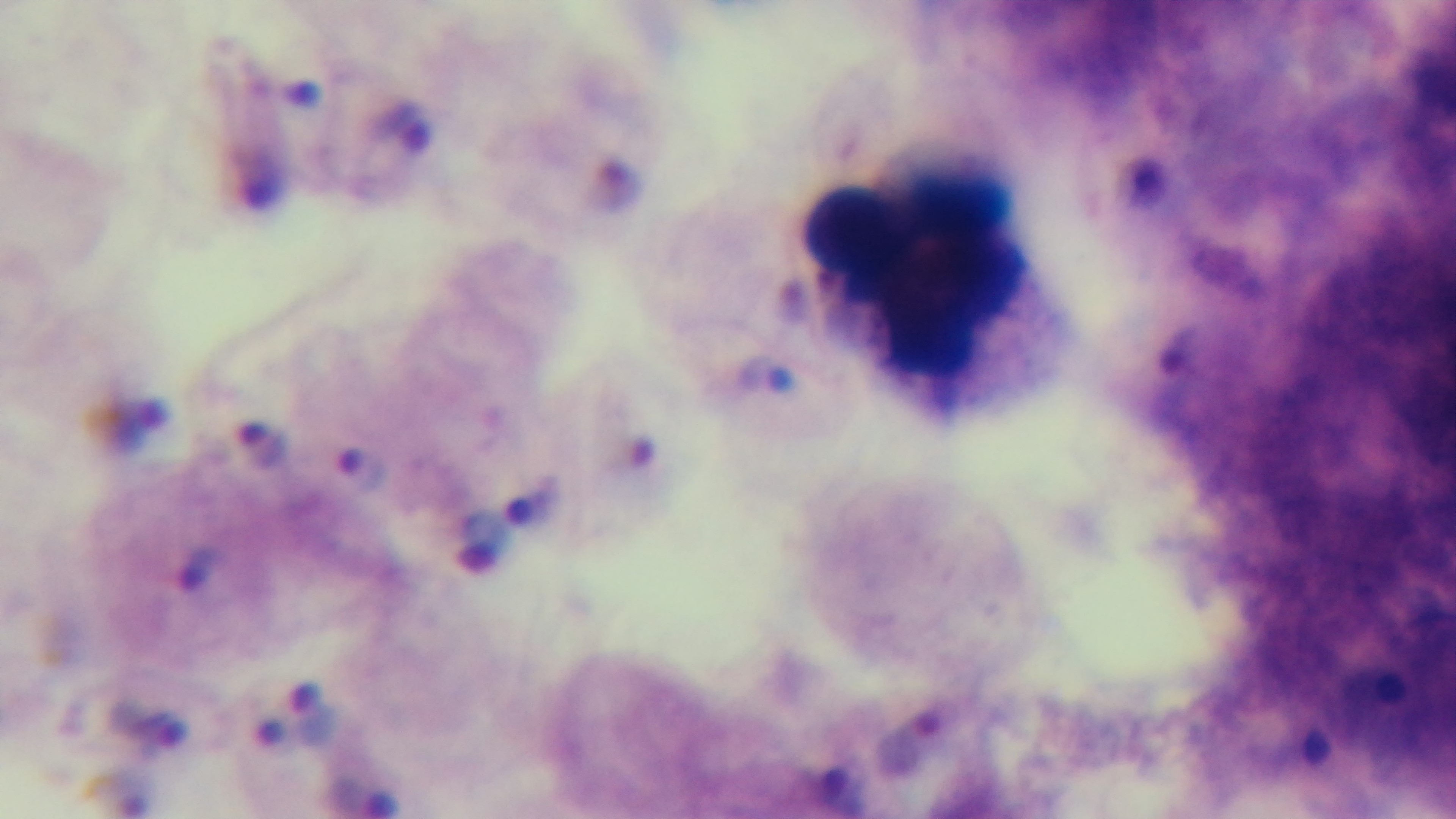

malaria_status: infected
preparation: thick smear
objective: 100x oil immersion
modality: light microscopy
capture: mounted 4K digital camera
field_of_view: one from the slide
stain: Giemsa